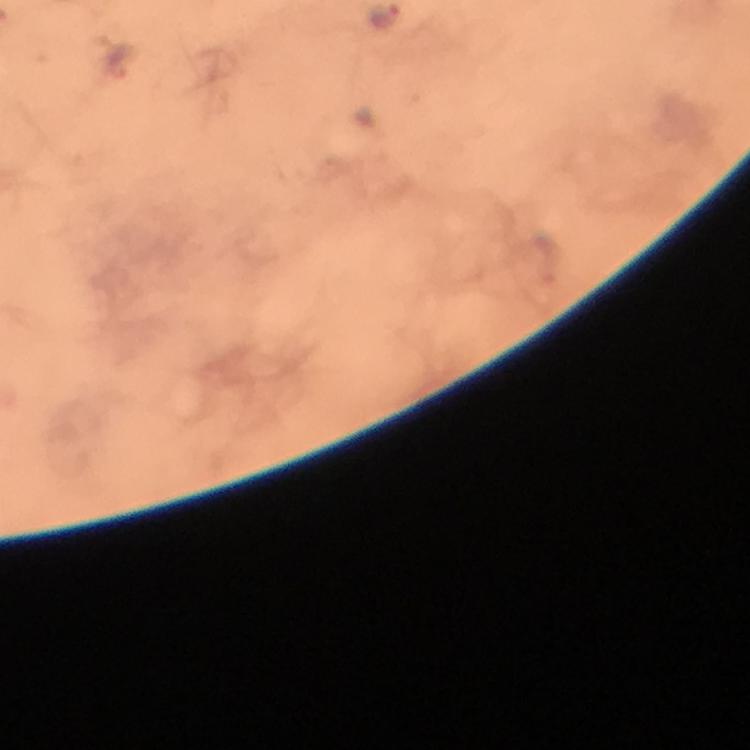

immersion oil = applied
image size = 750×750 pixels
capture = smartphone photograph through a microscope
preparation = thick blood smear
magnification = 100x
malaria parasite locations = approximate centers as [x, y] in pixels: [120, 60]
cropped from = a single field of view
context = from a malaria diagnostic workup
stain = Giemsa